Assess this cell for malaria.
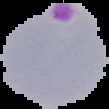
It is parasitized.

preparation: thin blood smear
image_size: 109×109 pixels
image_type: segmented cell region with the area outside set to black